Draw a bounding box around every leukocyte (white blood cell).
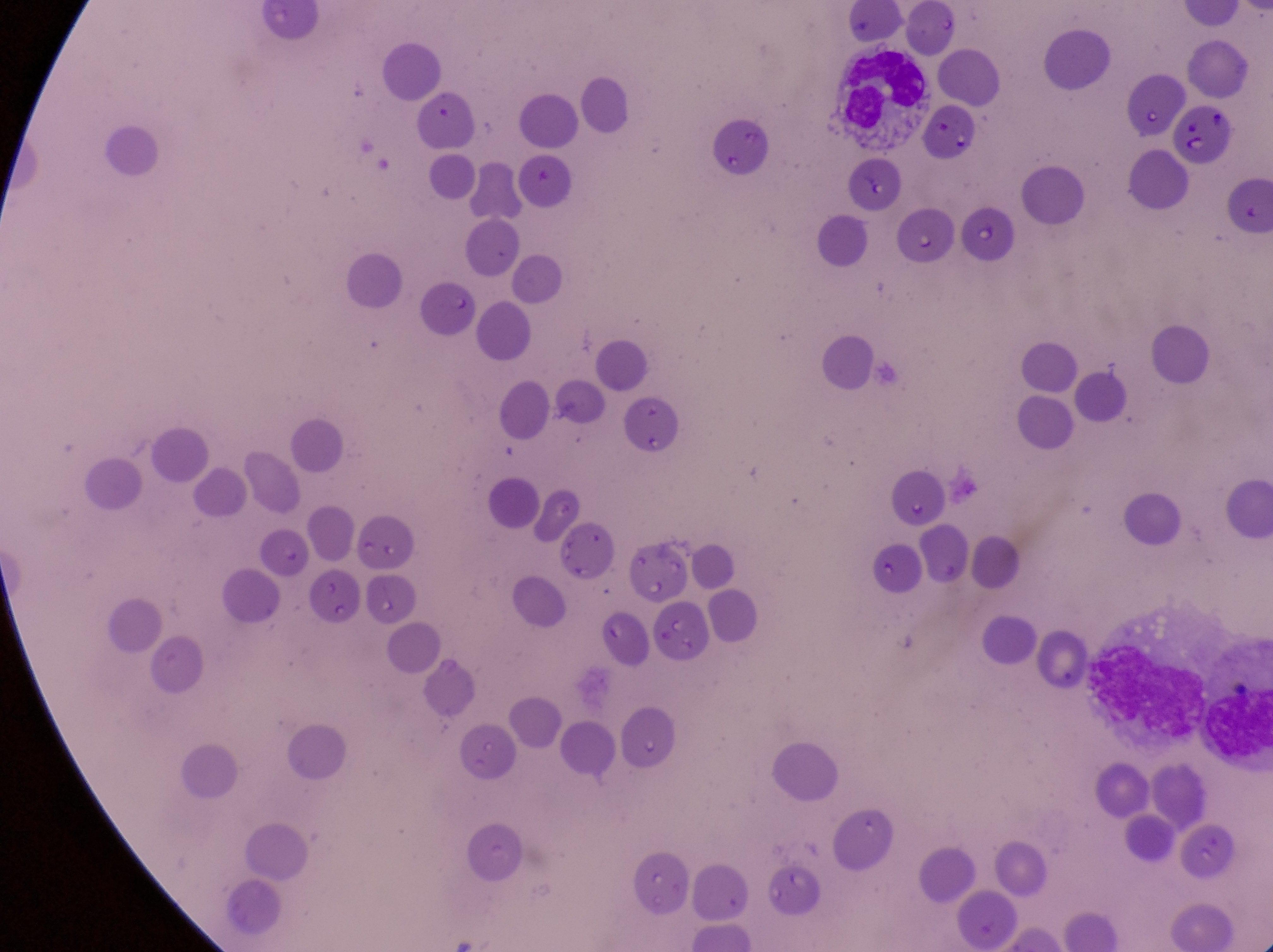

Approximate bounding boxes as {left, top, right, bottom} in pixels.
Leukocytes: {824, 42, 931, 139}, {1087, 632, 1205, 747}.

field of view = single
image size = 1273×952 pixels
parasitised red blood cell locations = approximate bounding boxes as {left, top, right, bottom} in pixels: {1171, 100, 1231, 162}, {969, 202, 1022, 269}, {899, 209, 951, 264}
artifact (platelet-like body, stain precipitate, or debris) locations = approximate bounding boxes as {left, top, right, bottom} in pixels: {517, 157, 562, 199}
magnification = 1000x
country = Uganda
preparation = thin blood film
capture = smartphone photograph through the eyepiece of an Olympus CX-23 microscope